Name the parasite shown.
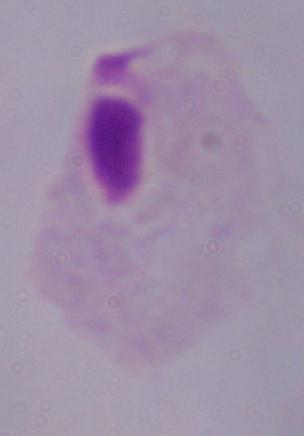
A trichomonad.

{
  "modality": "photomicrograph",
  "magnification": "1000x"
}